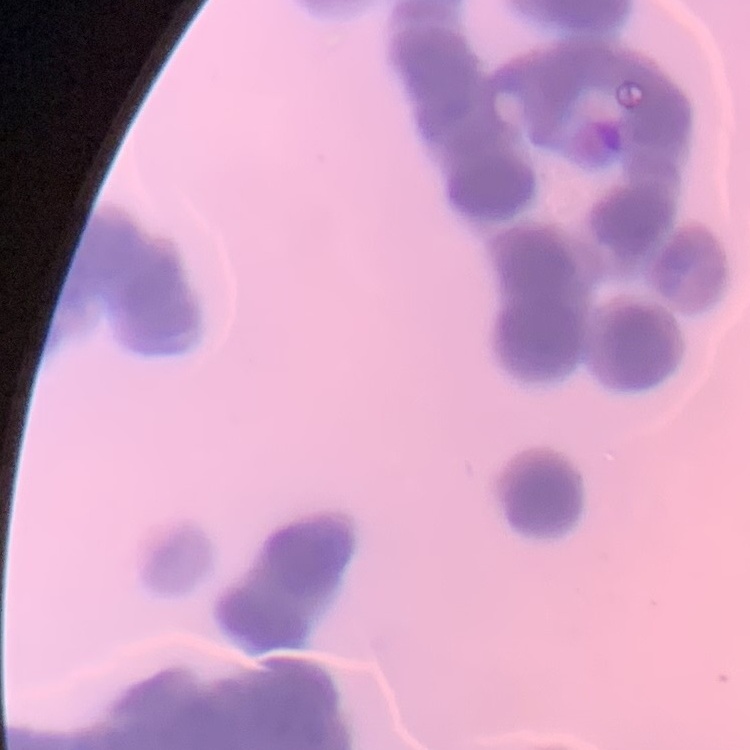

Summary:
  - Red blood cell morphology: rouleaux formation
  - Stain: Field's or Giemsa
  - Image type: one tile cut from a larger photomicrograph
  - Preparation: thin blood film